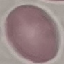

{
  "result": "no malaria parasites detected",
  "stain": "Giemsa",
  "preparation": "thin blood smear",
  "capture": "smartphone through the microscope eyepiece",
  "image_type": "cell patch, automatically extracted from a larger field of view and resized to 64 × 64 pixels"
}